Assess the morphology of the erythrocytes.
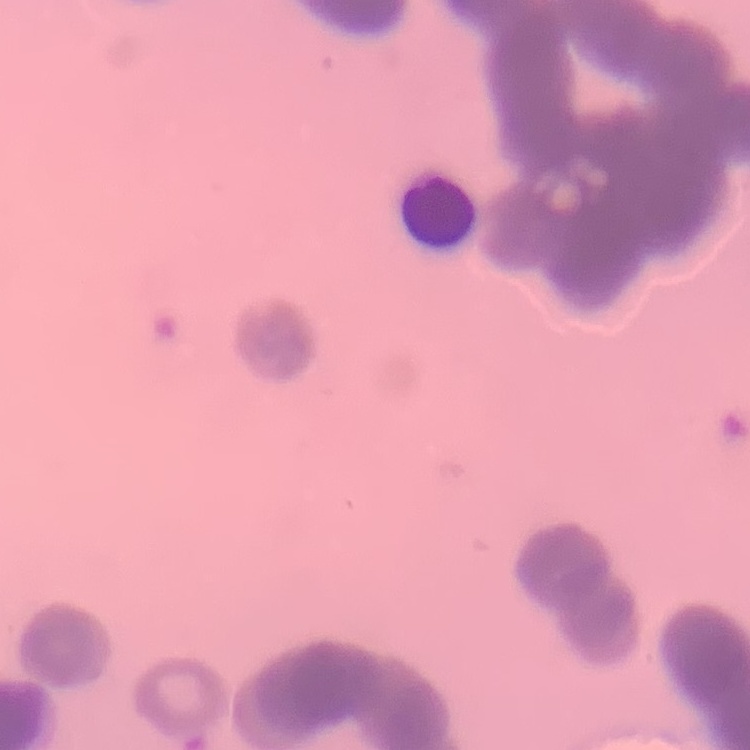

They show rouleaux formation.

preparation = thin blood film
stain = Field's or Giemsa
image type = one tile cut from a larger photomicrograph